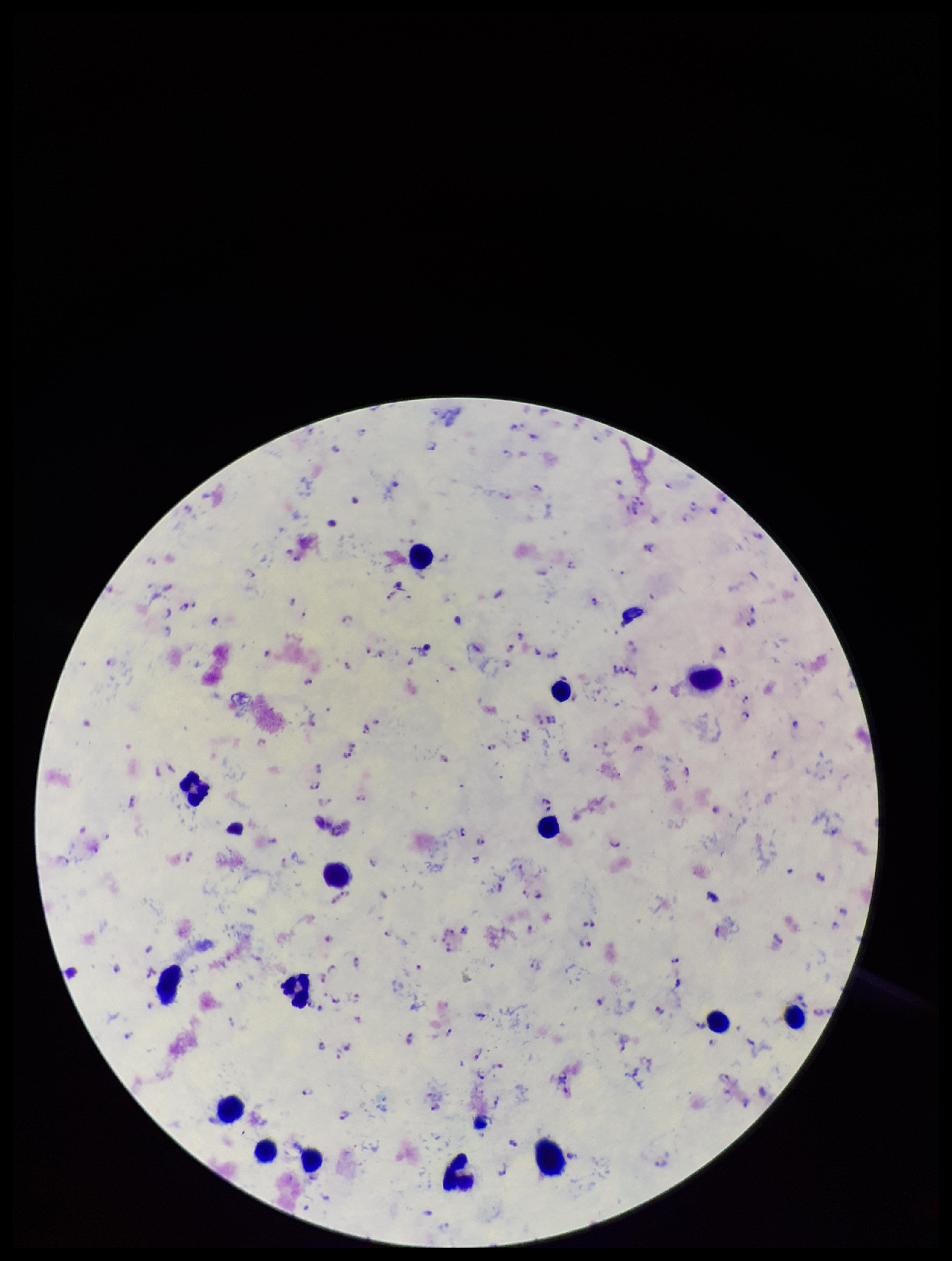
leukocyte_count: 15
field_of_view: one from this slide
capture: smartphone photograph through the microscope eyepiece
stain: Giemsa
image_size: 952×1261 pixels
species_reported_for_this_patient: Plasmodium falciparum
patient_malaria_status: positive
preparation: thick smear
plasmodium_parasites: identified
parasite_count: 118